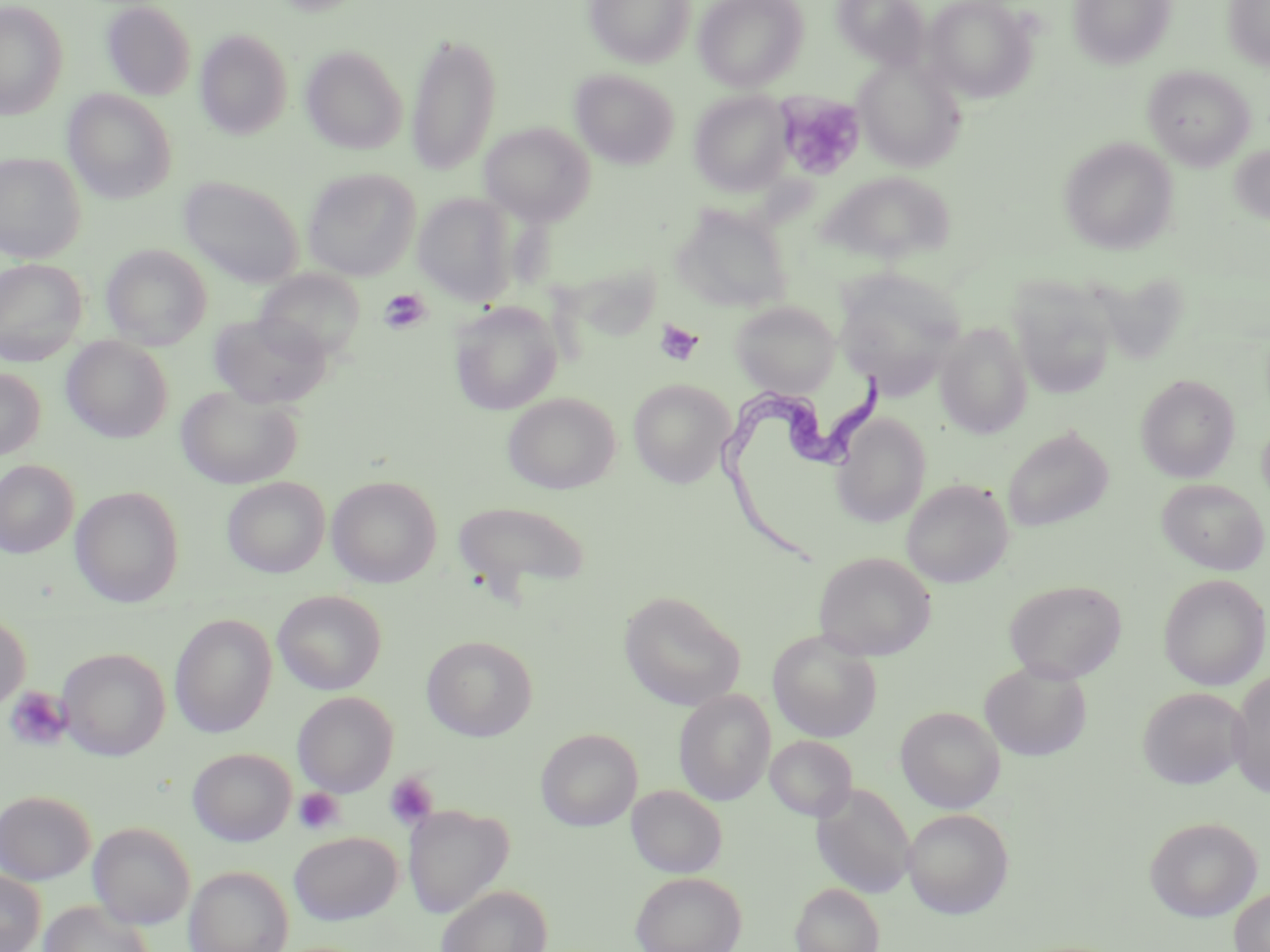
slide_level_diagnosis: Trypanosoma brucei
stain: May-Grünwald-Giemsa
modality: optical microscopy
image_size: 1270×952 pixels
field_of_view: single
trypanosoma_brucei_locations: 'approximate bounding boxes as (x1,y1)-(x2,y2) corner pairs in pixels: (713,365)-(890,568)'
platelet_locations: 'approximate bounding boxes as (x1,y1)-(x2,y2) corner pairs in pixels: (778,94)-(865,180), (378,288)-(430,335), (654,320)-(705,367), (5,687)-(72,751), (385,772)-(439,830), (293,788)-(344,835)'
uninfected_red_blood_cell_locations: 'approximate bounding boxes as (x1,y1)-(x2,y2) corner pairs in pixels: (584,0)-(696,68), (693,0)-(808,91), (831,0)-(931,70), (922,0)-(1035,102), (1067,0)-(1176,68), (1223,0)-(1270,70), (0,2)-(68,120), (101,2)-(196,100), (195,29)-(293,140), (406,32)-(502,176), (301,45)-(407,155), (853,57)-(965,171), (1143,65)-(1255,170), (570,69)-(679,169), (63,89)-(177,203), (689,90)-(794,196), (480,122)-(595,225), (1059,136)-(1179,255), (1229,143)-(1270,226), (0,152)-(86,262), (302,168)-(420,280), (178,176)-(305,288), (821,181)-(954,258), (413,193)-(517,306), (671,204)-(794,316), (101,244)-(212,349), (0,258)-(87,365), (833,268)-(966,396), (253,269)-(366,363), (1010,285)-(1118,399), (729,300)-(841,396), (450,302)-(563,415), (209,311)-(332,410), (936,323)-(1032,439), (62,336)-(173,443), (0,367)-(45,460), (1136,374)-(1240,482), (628,379)-(733,487), (176,384)-(302,489), (503,392)-(620,494), (833,413)-(931,528), (1257,417)-(1270,512), (1002,426)-(1114,533), (0,459)-(78,558), (327,475)-(442,588), (222,477)-(330,578), (1157,478)-(1269,575), (901,479)-(1013,588), (70,486)-(185,607), (452,500)-(592,600), (813,552)-(936,661), (1158,573)-(1269,691), (1003,579)-(1127,683), (272,590)-(386,695), (619,591)-(745,711), (0,612)-(31,712), (169,614)-(277,738), (767,630)-(883,742), (421,635)-(538,741), (58,647)-(170,761), (980,659)-(1092,761), (1228,669)-(1270,799), (1137,687)-(1248,789), (674,690)-(776,806), (293,692)-(398,797), (895,706)-(1005,813), (536,728)-(642,831), (765,735)-(857,821), (188,747)-(296,846), (811,783)-(915,899), (627,785)-(727,878), (0,789)-(95,884), (403,804)-(513,918), (903,807)-(1014,918), (1144,816)-(1262,922), (89,822)-(195,930), (288,831)-(402,925), (184,865)-(293,952), (0,870)-(45,952), (630,871)-(746,952), (790,883)-(884,952), (436,884)-(553,952), (1229,886)-(1270,952), (39,900)-(154,952)'
magnification: 1000x
preparation: thin blood smear